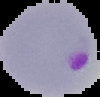 Malaria status: parasitized. From a thin blood smear. Image is 100×97 pixels. Segmented cell region on a black background.